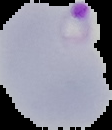

preparation = thin blood smear
image size = 112×130 pixels
image type = cell region segmented out of the field of view; surrounding area masked to black
result = Plasmodium parasites identified